Name the cell type shown.
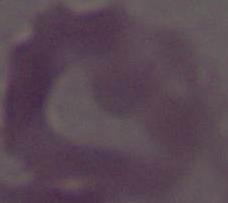
This is an erythrocyte.

1000x magnification. Photomicrograph.